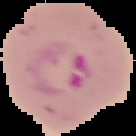

image type = segmented cell region on a black background
preparation = thin blood smear
image size = 136×136 pixels
malaria status = parasitized